Describe the morphology of the erythrocytes.
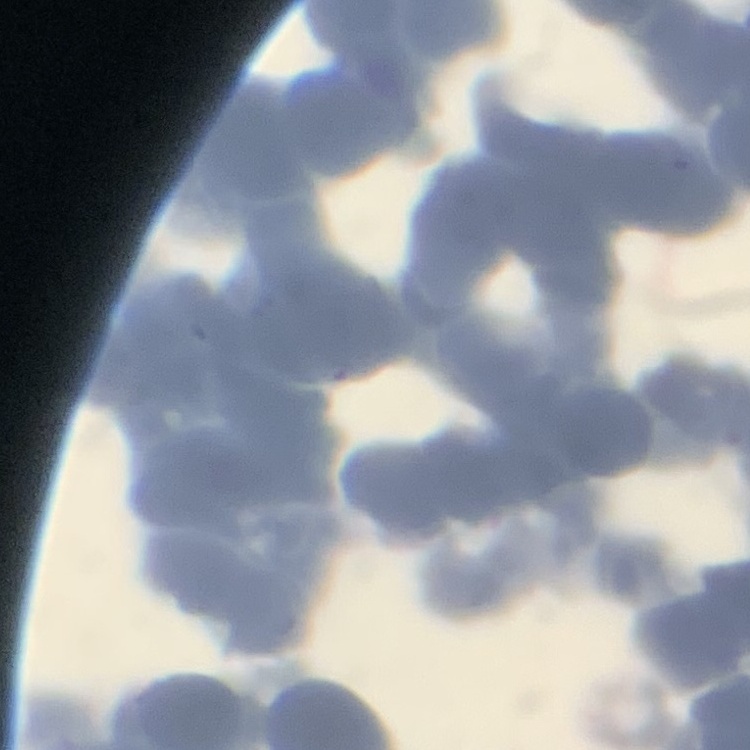

They show rouleaux formation.

Summary:
  - Preparation: thin peripheral smear
  - Stain: Field's or Giemsa
  - Image type: square crop of a larger photomicrograph